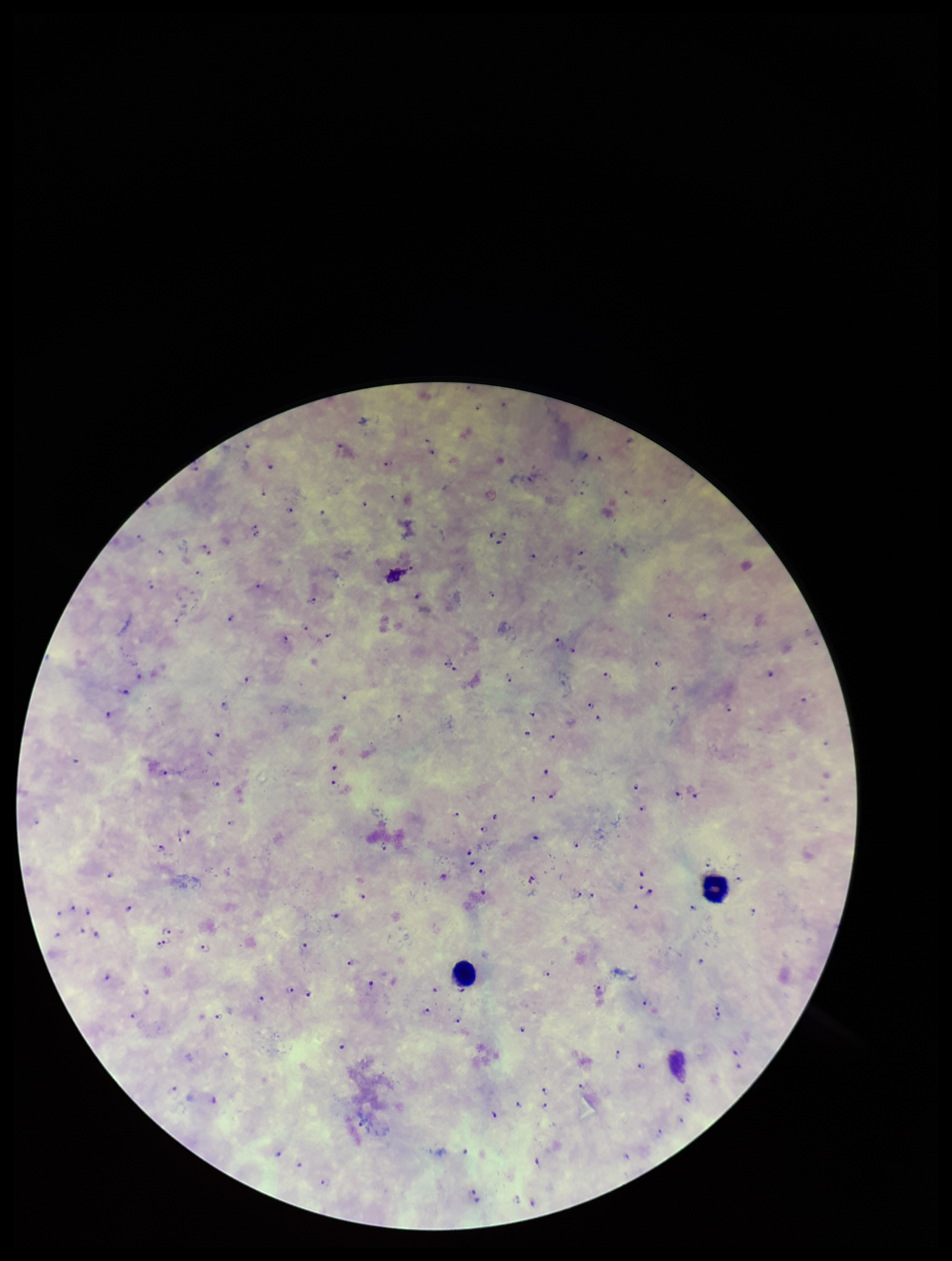
Summary:
  - Species reported for this patient: Plasmodium falciparum
  - Parasite count: 119
  - Field of view: single
  - Stain: Giemsa
  - Image size: 952×1261 pixels
  - Patient malaria status: infected
  - Preparation: thick smear
  - Plasmodium parasites: seen
  - Leukocyte count: 2
  - Capture: smartphone photograph through the microscope eyepiece